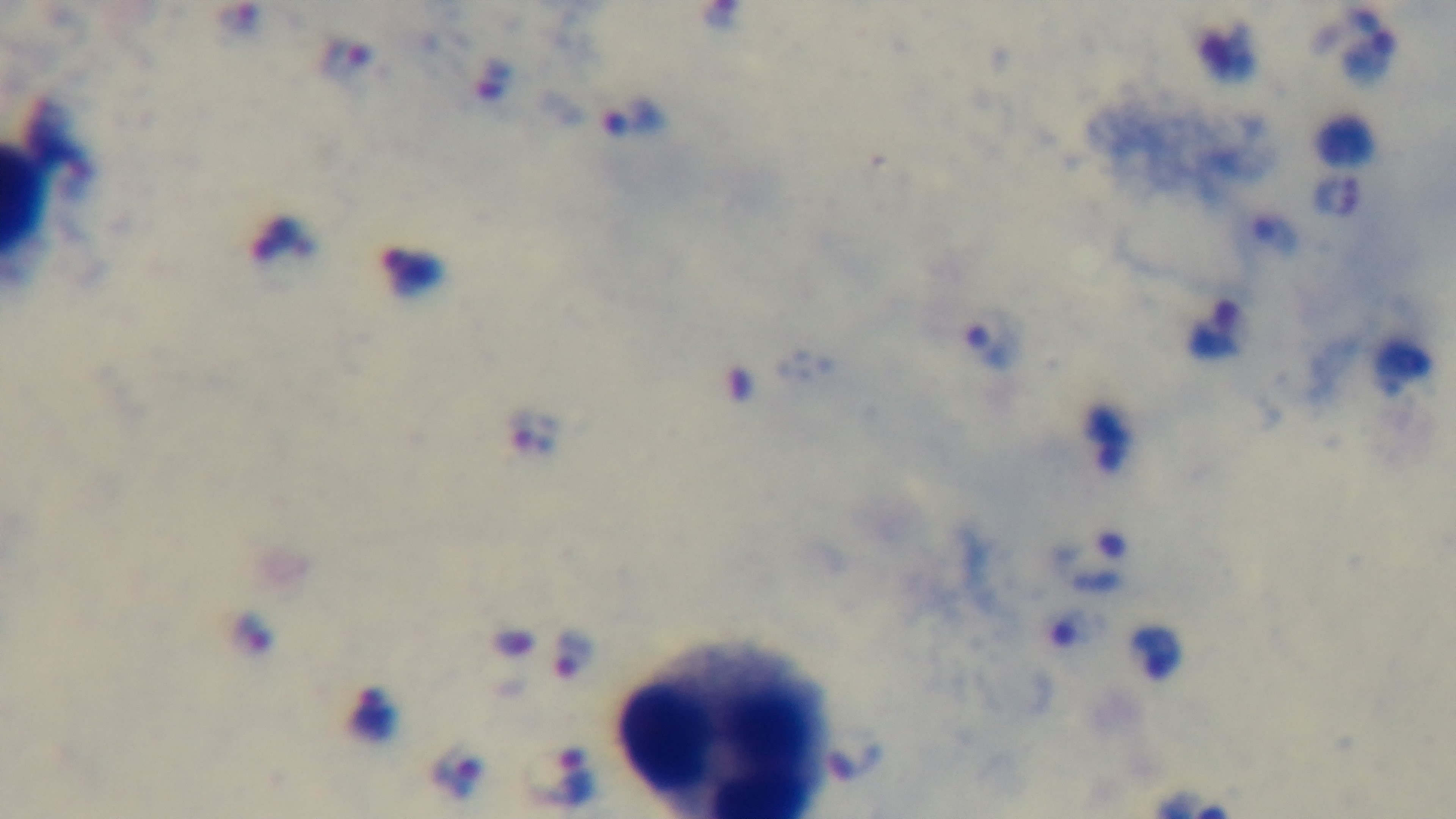

Oil-immersion objective, 100x. Preparation: thick blood film. Light microscopy. Malaria status: infected. Mounted 4K digital camera. Single field of view. Giemsa stain.